Locate and identify every blood parasite.
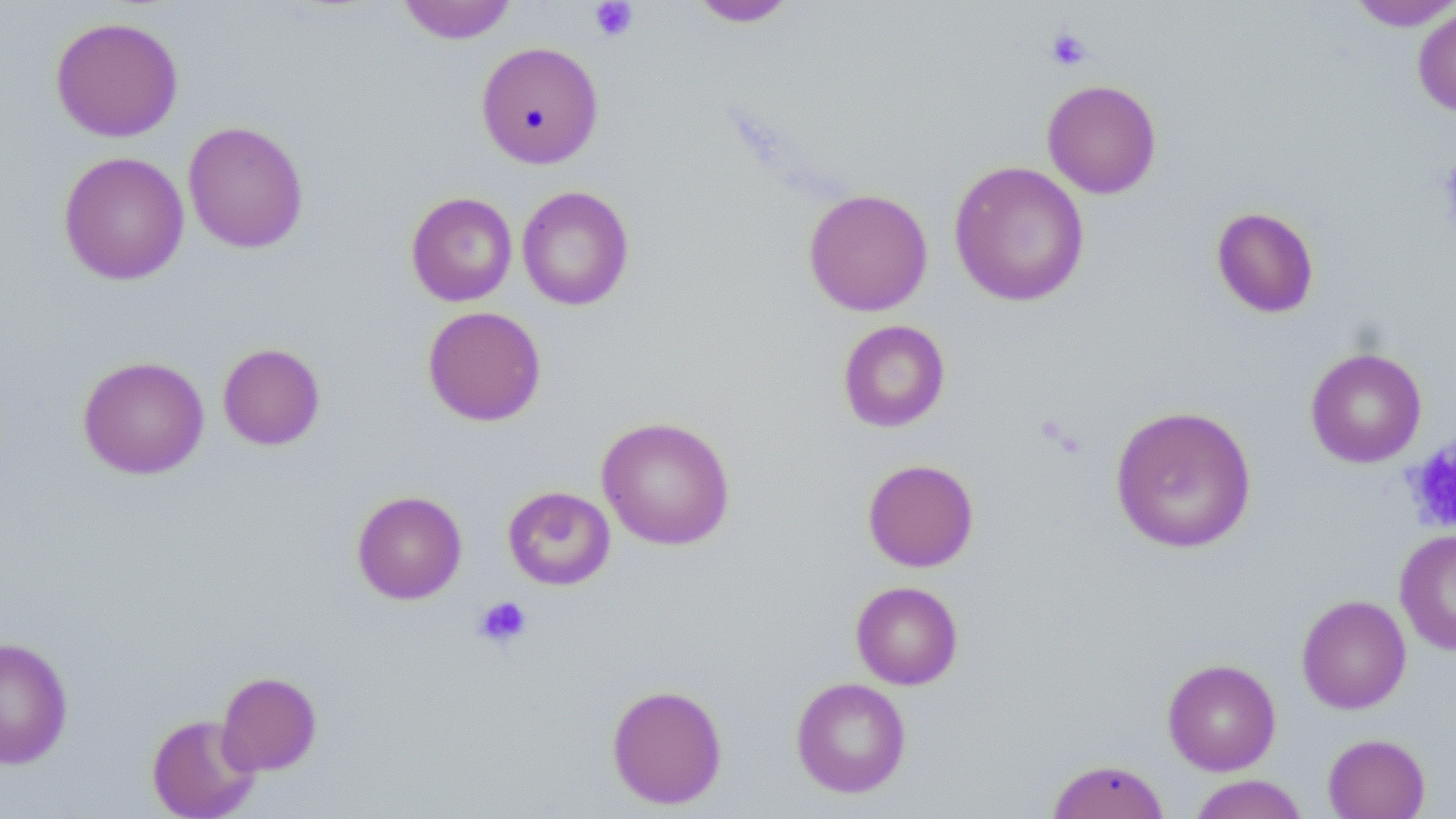

No blood parasites observed.

slide-level diagnosis = negative for blood parasites
preparation = thin blood film
field of view = single
platelet locations = approximate bounding boxes as (x1,y1)-(x2,y2) corner pairs in pixels: (589,1)-(638,42), (1045,28)-(1092,71), (1402,438)-(1456,534), (473,596)-(532,649)
uninfected red blood cell locations = approximate bounding boxes as (x1,y1)-(x2,y2) corner pairs in pixels: (396,0)-(517,44), (687,0)-(800,27), (1346,0)-(1456,31), (1412,4)-(1456,117), (50,15)-(184,142), (476,41)-(604,169), (1042,79)-(1162,198), (183,120)-(309,254), (58,151)-(189,285), (948,161)-(1090,307), (517,185)-(635,311), (803,188)-(933,316), (405,192)-(518,307), (1211,206)-(1320,318), (422,305)-(547,426), (837,319)-(950,433), (218,343)-(326,451), (1305,347)-(1427,468), (77,355)-(210,479), (1110,405)-(1257,553), (596,416)-(736,551), (862,458)-(979,572), (502,485)-(616,590), (352,490)-(467,604), (1395,528)-(1456,656), (850,581)-(963,689), (1296,594)-(1412,714), (0,637)-(73,769), (1163,658)-(1281,776), (216,671)-(322,776), (790,677)-(912,798), (606,683)-(728,809), (146,713)-(261,819), (1322,733)-(1431,819), (1046,759)-(1170,819), (1188,774)-(1310,819)
magnification = 1000x
image size = 1456×819 pixels
stain = May-Grünwald-Giemsa
modality = light microscopy